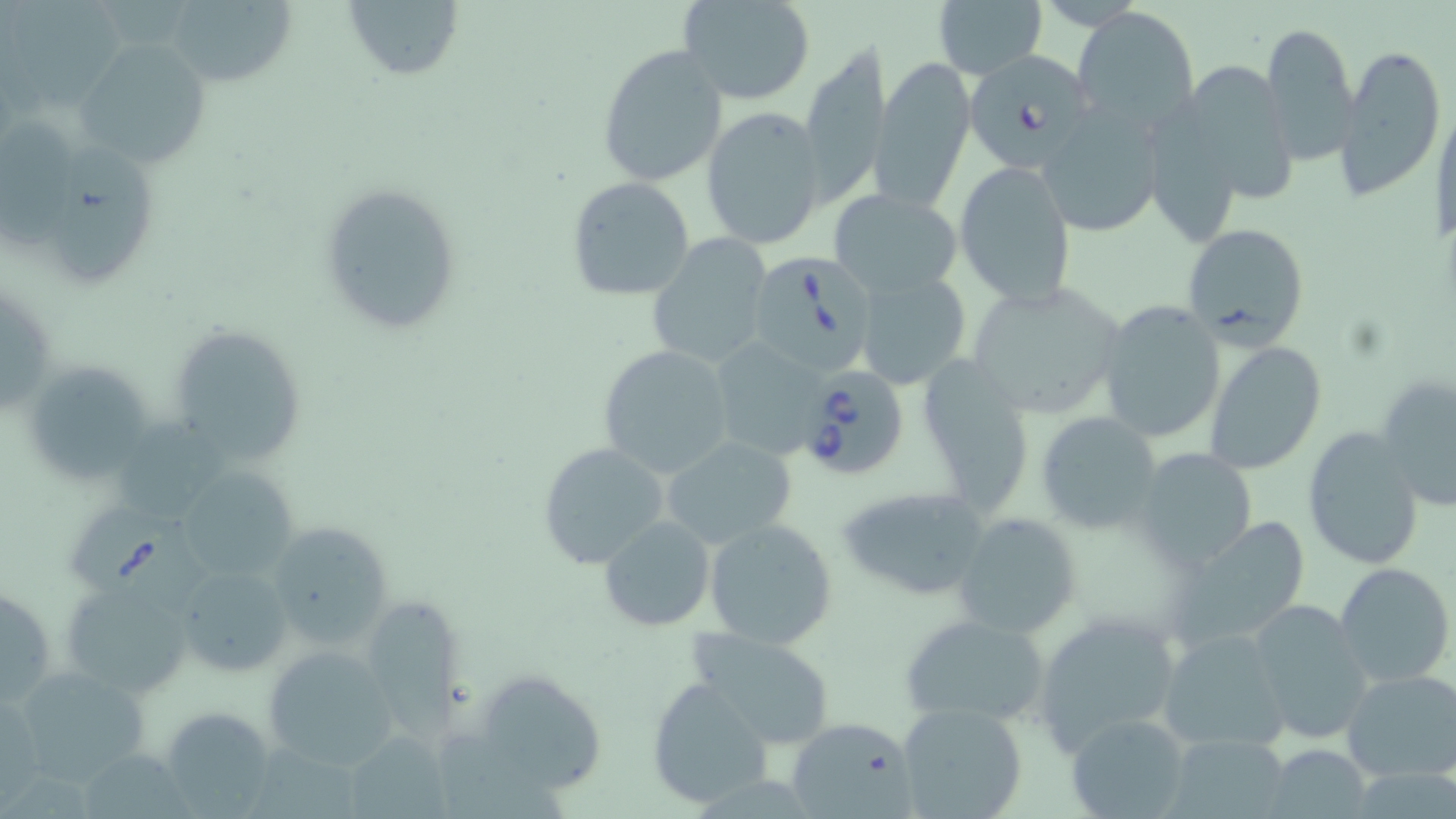

slide-level diagnosis = Babesia divergens
stain = May-Grünwald-Giemsa
field of view = single
image size = 1456×819 pixels
preparation = thin blood film
Babesia divergens-infected red blood cell locations = approximate bounding boxes as named x1/y1/x2/y2 corners in pixels: (x1=961, y1=48, x2=1098, y2=172), (x1=755, y1=257, x2=873, y2=371), (x1=795, y1=366, x2=910, y2=483), (x1=67, y1=513, x2=220, y2=617)
modality = optical microscopy
magnification = 1000x
uninfected red blood cell locations = approximate bounding boxes as named x1/y1/x2/y2 corners in pixels: (x1=165, y1=0, x2=295, y2=89), (x1=344, y1=0, x2=464, y2=84), (x1=679, y1=0, x2=815, y2=105), (x1=933, y1=1, x2=1047, y2=81), (x1=1075, y1=6, x2=1200, y2=132), (x1=1260, y1=19, x2=1362, y2=163), (x1=75, y1=39, x2=214, y2=171), (x1=595, y1=44, x2=729, y2=187), (x1=1338, y1=45, x2=1445, y2=202), (x1=799, y1=46, x2=891, y2=207), (x1=871, y1=55, x2=975, y2=212), (x1=1174, y1=57, x2=1300, y2=208), (x1=1038, y1=100, x2=1169, y2=237), (x1=1140, y1=100, x2=1257, y2=247), (x1=701, y1=107, x2=826, y2=252), (x1=3, y1=118, x2=91, y2=253), (x1=44, y1=142, x2=169, y2=287), (x1=954, y1=161, x2=1077, y2=306), (x1=565, y1=178, x2=695, y2=302), (x1=320, y1=181, x2=463, y2=334), (x1=829, y1=189, x2=963, y2=299), (x1=1180, y1=222, x2=1310, y2=348), (x1=648, y1=234, x2=775, y2=368), (x1=853, y1=271, x2=971, y2=391), (x1=963, y1=279, x2=1126, y2=422), (x1=1095, y1=298, x2=1227, y2=446), (x1=163, y1=319, x2=307, y2=466), (x1=708, y1=335, x2=833, y2=462), (x1=1203, y1=340, x2=1327, y2=476), (x1=597, y1=344, x2=736, y2=478), (x1=913, y1=351, x2=1034, y2=514), (x1=22, y1=358, x2=159, y2=488), (x1=1374, y1=373, x2=1456, y2=512), (x1=1036, y1=412, x2=1163, y2=530), (x1=1303, y1=428, x2=1426, y2=570), (x1=660, y1=436, x2=799, y2=550), (x1=536, y1=442, x2=672, y2=571), (x1=1134, y1=447, x2=1259, y2=570), (x1=174, y1=467, x2=303, y2=585), (x1=837, y1=485, x2=994, y2=602), (x1=952, y1=512, x2=1082, y2=639), (x1=1171, y1=514, x2=1313, y2=648), (x1=598, y1=516, x2=716, y2=633), (x1=703, y1=519, x2=840, y2=648), (x1=265, y1=521, x2=394, y2=650), (x1=1333, y1=560, x2=1454, y2=688), (x1=171, y1=562, x2=293, y2=674), (x1=61, y1=579, x2=195, y2=701), (x1=0, y1=581, x2=56, y2=711), (x1=358, y1=597, x2=463, y2=739), (x1=1246, y1=600, x2=1374, y2=743), (x1=1031, y1=609, x2=1184, y2=754), (x1=898, y1=612, x2=1049, y2=730), (x1=683, y1=627, x2=840, y2=750), (x1=1158, y1=628, x2=1292, y2=752), (x1=264, y1=643, x2=397, y2=770), (x1=10, y1=663, x2=150, y2=786), (x1=473, y1=667, x2=610, y2=797), (x1=1341, y1=669, x2=1456, y2=783), (x1=646, y1=678, x2=772, y2=809), (x1=0, y1=692, x2=44, y2=803), (x1=897, y1=701, x2=1029, y2=819), (x1=158, y1=705, x2=277, y2=815), (x1=1065, y1=712, x2=1191, y2=819), (x1=786, y1=715, x2=916, y2=817), (x1=345, y1=729, x2=451, y2=819), (x1=1165, y1=731, x2=1292, y2=819), (x1=1264, y1=743, x2=1373, y2=817)